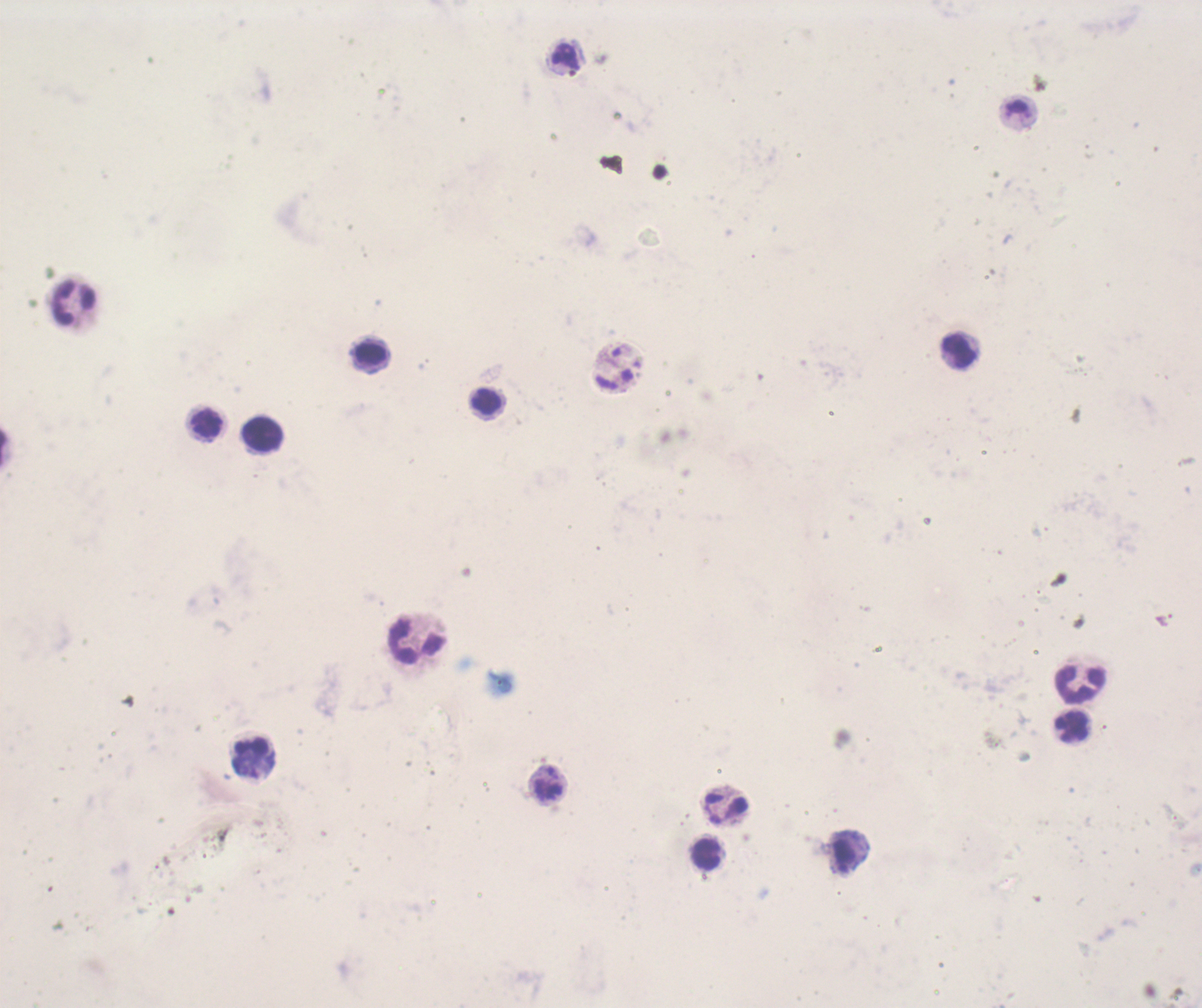
Approximate centers as (x, y) in pixels.
Summary:
  - Leukocyte locations: (74, 303), (959, 350), (371, 355), (487, 402), (206, 423), (262, 433), (417, 641), (1080, 684), (1072, 726), (253, 759), (548, 784), (726, 809), (707, 854)
  - Trophozoite locations: (565, 56), (845, 856)
  - Image size: 1202×1008 pixels
  - Preparation: thick smear of blood
  - Field of view: single
  - Background quality: unsatisfactory
  - Result: positive for malaria parasites
  - Magnification: 100x
  - Context: previously used in a real diagnosis
  - Coloration quality: bad
  - Stain: Romanowsky